Assess this cell for malaria.
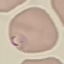

Parasitized.

image type = cell patch, automatically extracted from a larger field of view and resized to 64 × 64 pixels
capture = smartphone camera at the microscope eyepiece
stain = Giemsa
preparation = thin blood smear